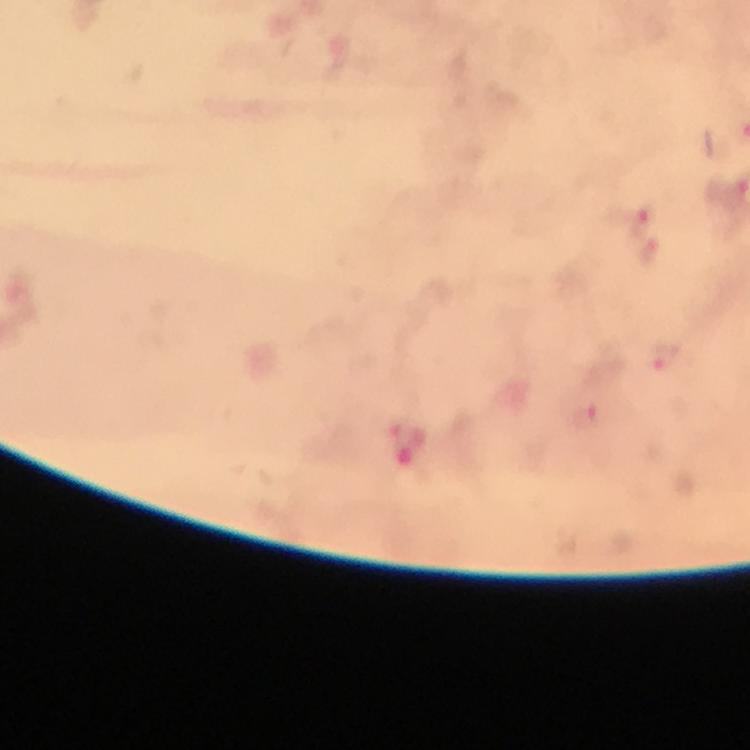 Approximate object centers, in pixels from the top-left corner. Malaria parasite locations: (x=626, y=189), (x=661, y=354). From a diagnostic examination for malaria. 100x magnification. Image is 750×750 pixels. Thick smear. Photographed with a smartphone mounted on the microscope. Cropped region of a single field of view. Giemsa-stained preparation. Immersion oil was used.